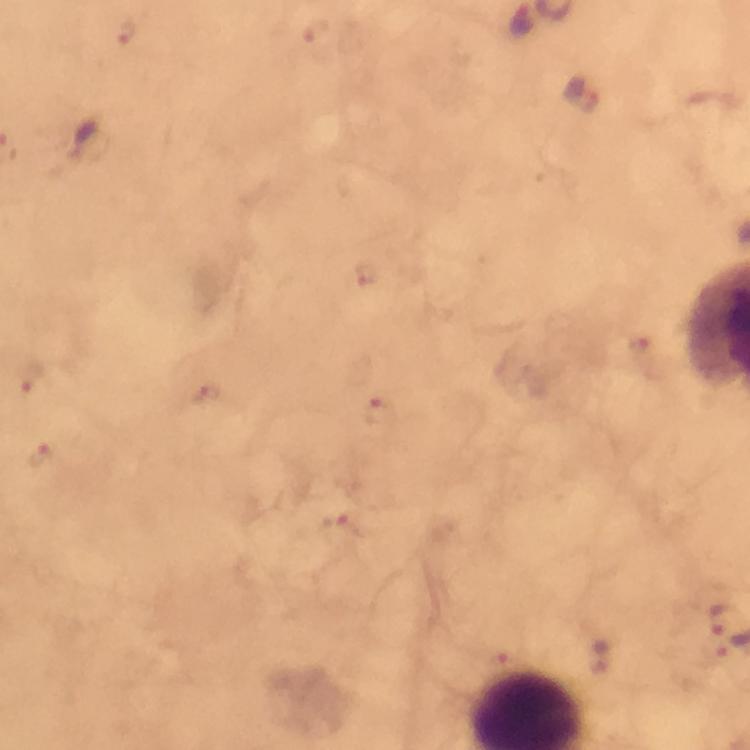 Approximate centers as {x, y} in pixels. Plasmodium parasite locations: {126, 33}, {582, 95}, {368, 276}, {642, 348}, {31, 374}, {208, 394}, {376, 410}, {40, 456}, {340, 532}, {720, 617}, {498, 665}. Photographed with a smartphone mounted on the microscope. At 100x magnification. Giemsa stain. From a malaria diagnostic workup. A crop from one field of view. Image is 750×750 pixels. Immersion oil was used. Thick smear.